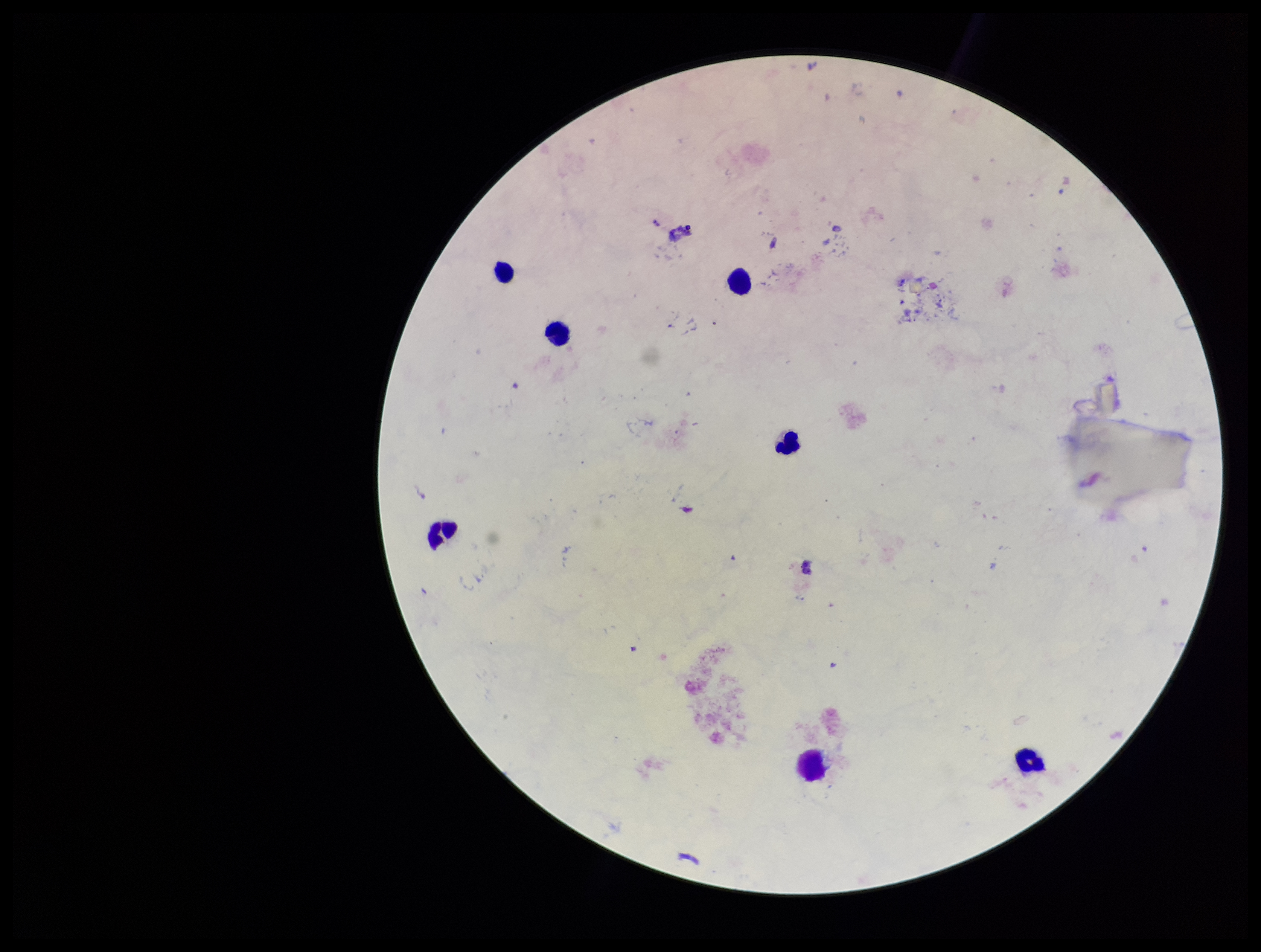
patient malaria status = negative
capture = smartphone photograph through the microscope eyepiece
preparation = thick blood smear
field of view = one from this slide
image size = 1261×952 pixels
stain = Giemsa
Plasmodium parasites = none detected
leukocyte count = 7
parasite count = 0